Report the malaria status of this cell.
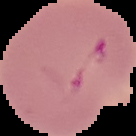
Parasitized.

Cell region segmented out of the field of view; the surrounding area is masked to black. From a thin blood smear. Image is 136×136 pixels.